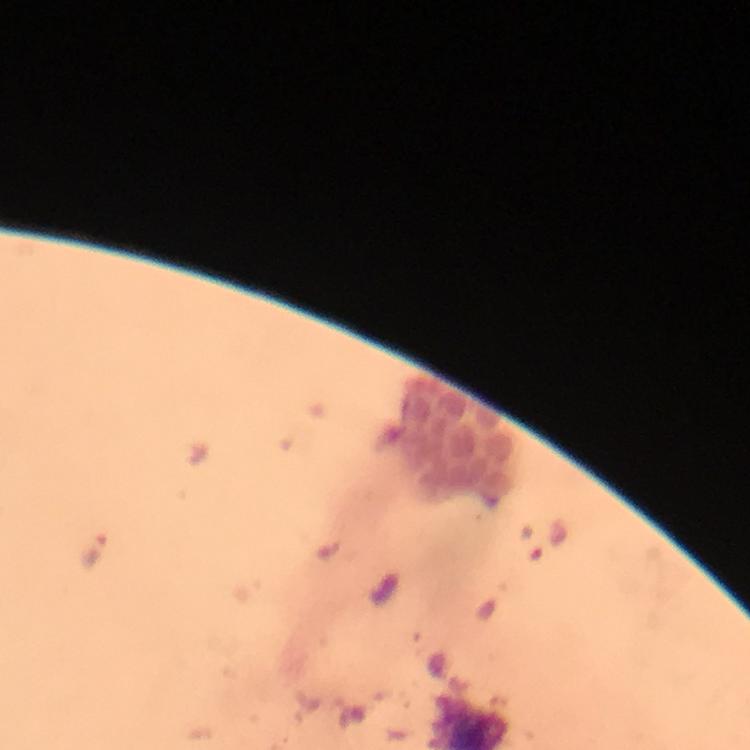

Approximate centers as {x, y} in pixels.
Summary:
  - Plasmodium parasite locations: {93, 550}
  - Stain: Giemsa
  - Capture: smartphone photograph through a microscope
  - Context: from a malaria diagnostic workup
  - Cropped from: a single field of view
  - Image size: 750×750 pixels
  - Magnification: 100x
  - Immersion oil: used
  - Preparation: thick smear